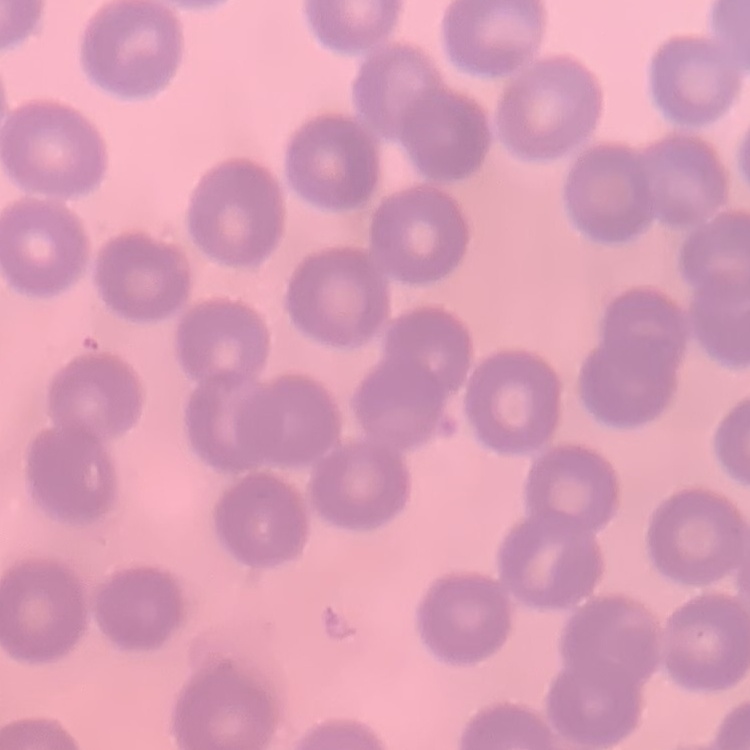

The red blood cells show no rouleaux formation. Thin peripheral smear. One tile cut from a larger photomicrograph. Field's or Giemsa stain.